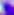

modality = photomicrograph
identification = Toxoplasma gondii
magnification = 400x